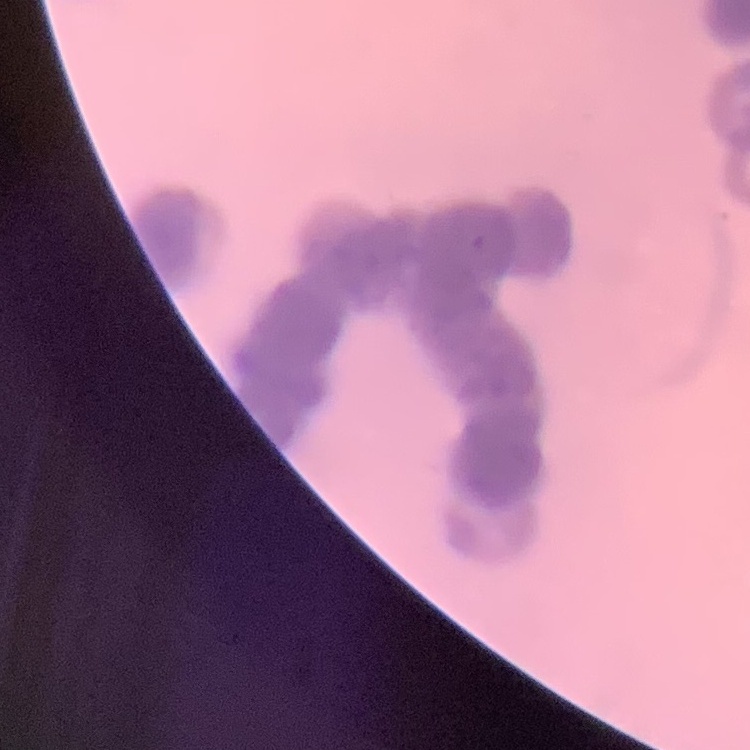
Summary:
  - Erythrocyte morphology: rouleaux formation
  - Preparation: thin peripheral smear
  - Stain: Field's or Giemsa
  - Image type: square crop of a larger photomicrograph